Assess this cell for malaria.
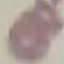

Uninfected.

image type = automatically extracted cell patch, resized to 64 × 64 pixels
preparation = thin blood smear
capture = smartphone camera at the microscope eyepiece
stain = Giemsa